Assess this cell for malaria.
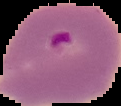
Parasitized.

image type = cell region segmented out of the field of view; surrounding area masked to black
image size = 121×106 pixels
preparation = thin blood film